Classify this cell by malaria status.
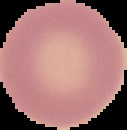

Uninfected.

Summary:
  - Preparation: thin blood smear
  - Image size: 127×130 pixels
  - Image type: cell region segmented out of the field of view; surrounding area masked to black